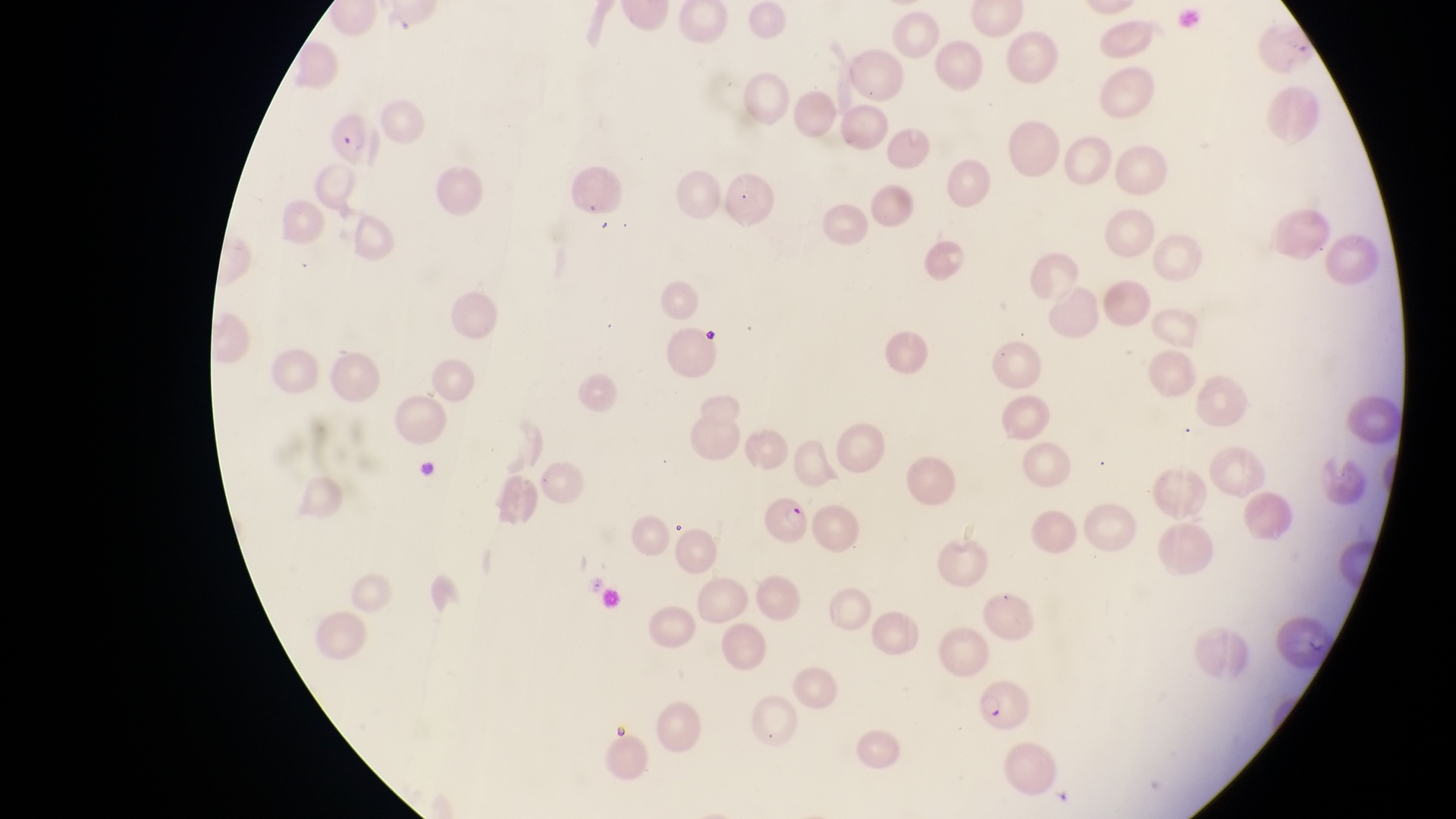
Approximate bounding boxes as {left, top, right, bottom} in pixels.
Summary:
  - Parasitised red blood cell locations: {320, 105, 386, 168}, {759, 497, 823, 560}, {971, 680, 1030, 735}
  - Preparation: thin blood smear
  - Magnification: 1000x
  - Capture: smartphone photograph through the eyepiece of an Olympus CX-23 microscope
  - Country: Uganda
  - Field of view: single
  - Image size: 1456×819 pixels